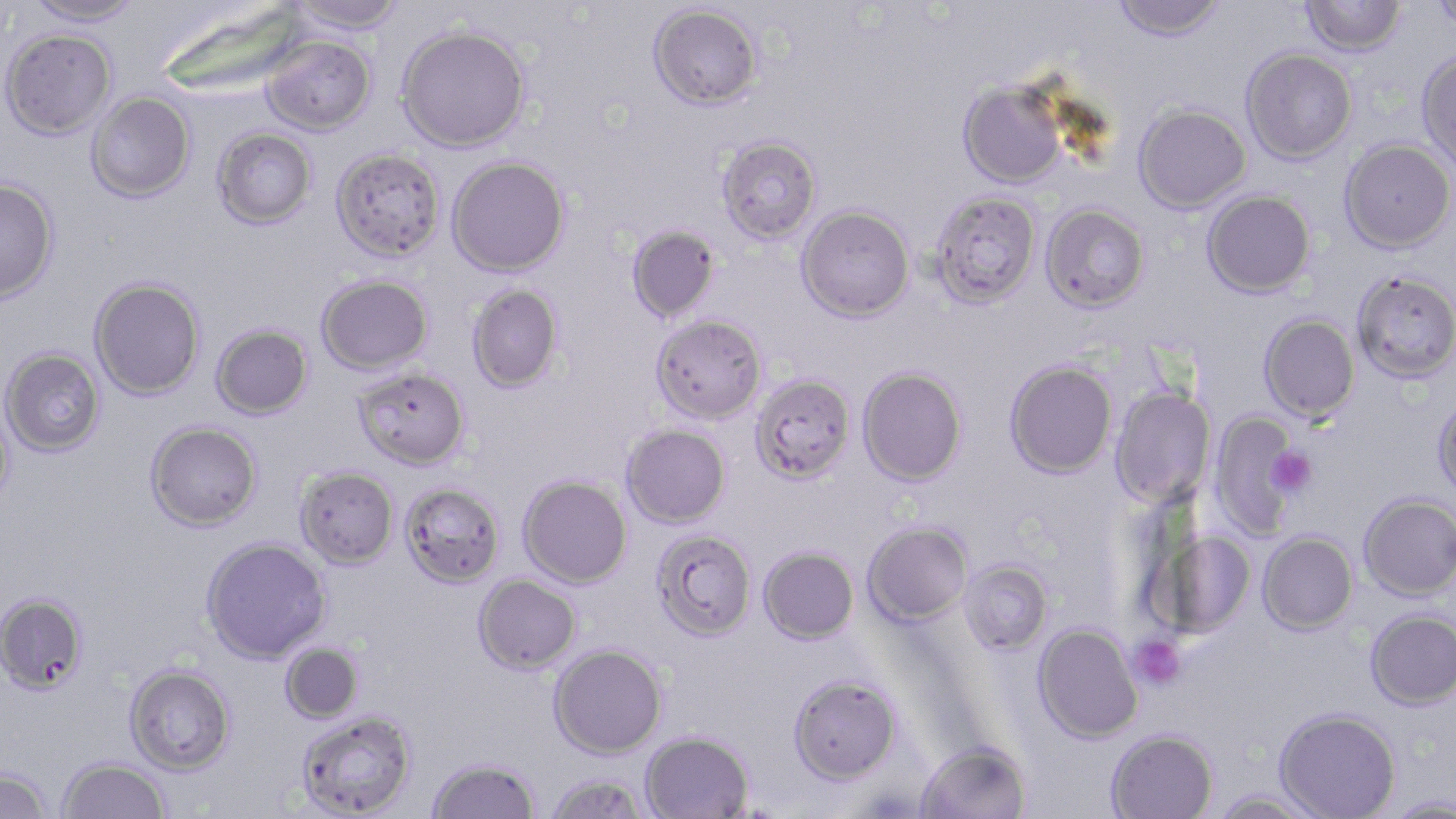
Summary:
  - Coordinate format: approximate bounding boxes as (x1, y1, x2, y2) in pixels
  - Platelet locations: (1266, 447, 1317, 496), (1128, 634, 1186, 691)
  - Uninfected red blood cell locations: (24, 0, 144, 27), (286, 0, 406, 35), (1111, 0, 1227, 42), (1299, 0, 1407, 56), (1426, 2, 1456, 30), (648, 3, 763, 111), (396, 24, 531, 152), (1, 28, 116, 140), (261, 35, 376, 135), (1241, 48, 1357, 164), (1416, 49, 1456, 171), (958, 80, 1068, 188), (86, 92, 195, 203), (1133, 104, 1251, 213), (212, 127, 317, 229), (716, 135, 822, 244), (1339, 138, 1455, 253), (331, 147, 445, 262), (447, 156, 570, 277), (0, 178, 59, 304), (1202, 190, 1315, 298), (930, 191, 1041, 307), (1040, 202, 1150, 312), (797, 205, 915, 322), (627, 225, 720, 323), (1351, 270, 1456, 383), (316, 273, 433, 375), (89, 277, 205, 400), (466, 283, 564, 393), (651, 313, 767, 424), (1258, 313, 1360, 423), (211, 324, 313, 420), (1, 347, 106, 456), (1004, 360, 1117, 478), (353, 366, 470, 470), (857, 366, 968, 486), (751, 374, 856, 483), (1109, 386, 1216, 507), (0, 393, 16, 515), (1433, 393, 1456, 500), (1210, 412, 1305, 537), (145, 421, 263, 532), (621, 424, 731, 528), (294, 466, 399, 568), (518, 475, 632, 588), (400, 482, 505, 588), (1359, 493, 1456, 601), (862, 521, 972, 626), (1150, 528, 1256, 640), (651, 529, 757, 641), (1258, 531, 1358, 634), (200, 537, 331, 664), (758, 546, 858, 644), (960, 560, 1052, 654), (473, 574, 581, 674), (0, 591, 89, 695), (1365, 609, 1456, 710), (1033, 623, 1143, 743), (279, 642, 363, 724), (549, 644, 666, 759), (124, 664, 236, 774), (788, 673, 901, 785), (1274, 708, 1401, 818), (295, 709, 418, 819), (1107, 729, 1217, 819), (641, 730, 754, 819), (915, 740, 1031, 819), (427, 757, 540, 819), (57, 758, 171, 818), (0, 767, 52, 819), (544, 772, 652, 819), (1210, 791, 1325, 818), (1383, 795, 1456, 818)
  - Slide-level diagnosis: Plasmodium falciparum
  - Field of view: one of a larger specimen
  - Modality: optical microscopy
  - Image size: 1456×819 pixels
  - Magnification: 1000x
  - Preparation: thin blood smear
  - Stain: May-Grünwald-Giemsa